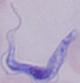 A trypanosome is seen. Captured at 1000x magnification. Micrograph.